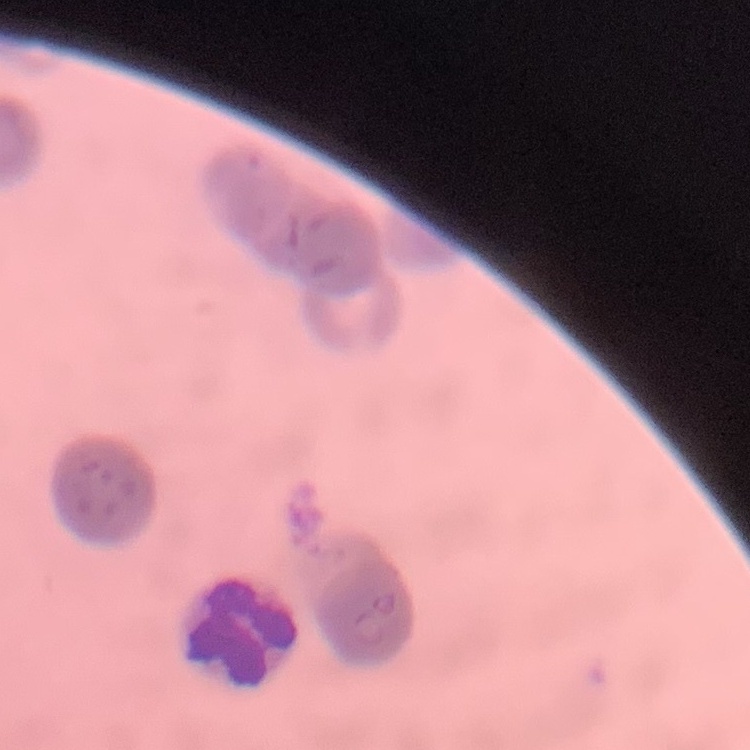

red_blood_cell_morphology: rouleaux formation
stain: Field's or Giemsa
preparation: thin blood smear
image_type: one tile cut from a larger photomicrograph